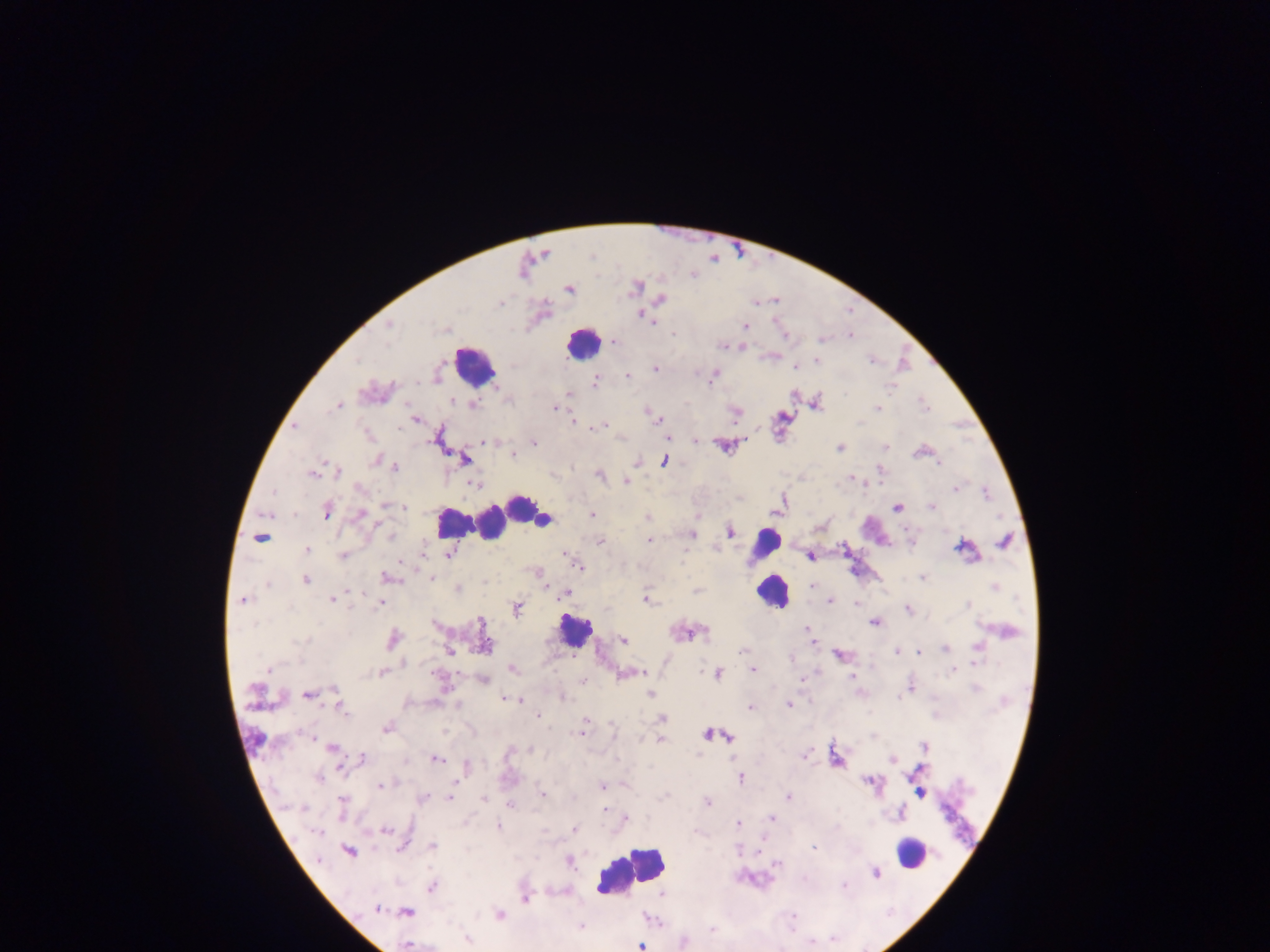
Approximate centers as [x, y] in pixels.
Summary:
  - Plasmodium parasite locations: [592, 256], [634, 287], [569, 289], [661, 299], [500, 303], [643, 316], [650, 321], [389, 325], [745, 326], [785, 335], [850, 335], [821, 339], [613, 341], [721, 346], [816, 360], [357, 361], [871, 361], [656, 368], [794, 368], [713, 375], [627, 376], [595, 382], [891, 387], [567, 395], [452, 402], [474, 404], [817, 404], [924, 405], [337, 406], [555, 409], [877, 409], [649, 412], [734, 413], [655, 417], [415, 420], [573, 420], [602, 426], [295, 427], [667, 437], [696, 441], [485, 442], [533, 443], [724, 445], [886, 446], [840, 447], [513, 455], [464, 460], [376, 461], [665, 461], [939, 464], [395, 467], [880, 470], [337, 472], [312, 473], [600, 475], [852, 478], [626, 481], [474, 484], [360, 489], [955, 489], [272, 492], [986, 493], [388, 506], [931, 507], [404, 508], [898, 508], [327, 512], [592, 514], [361, 515], [267, 516], [647, 518], [820, 526], [731, 532], [691, 534], [390, 535], [259, 538], [600, 541], [649, 541], [1004, 542], [962, 548], [307, 550], [424, 553], [342, 555], [449, 555], [566, 556], [809, 556], [578, 566], [386, 576], [431, 577], [923, 577], [306, 580], [267, 586], [813, 586], [995, 587], [457, 589], [567, 593], [332, 600], [647, 600], [243, 601], [830, 602], [380, 603], [857, 604], [969, 604], [517, 608], [908, 609], [874, 623], [435, 625], [484, 627], [808, 630], [392, 639], [485, 640], [622, 640], [299, 642], [811, 642], [978, 647], [945, 648], [742, 651], [449, 652], [896, 652], [920, 652], [839, 655], [512, 668], [269, 669], [752, 669], [953, 670], [381, 672], [633, 673], [718, 673], [852, 677], [484, 680], [583, 681], [908, 686], [975, 688], [335, 690], [651, 694], [308, 695], [563, 697], [507, 699], [788, 705], [750, 707], [342, 710], [538, 716], [663, 718], [585, 724], [386, 729], [582, 730], [614, 730], [708, 734], [309, 736], [728, 737], [660, 740], [924, 746], [332, 747], [529, 750], [805, 755], [363, 757], [437, 759], [892, 759], [467, 766], [919, 768], [319, 777], [741, 778], [870, 781], [381, 785], [603, 786], [542, 794], [919, 794], [665, 795], [451, 796], [788, 796], [423, 798], [483, 799], [342, 802], [707, 802], [511, 805], [303, 808], [605, 811], [901, 813], [626, 818], [771, 818], [738, 824], [498, 826], [575, 829], [385, 831], [318, 832], [401, 847], [433, 847], [814, 847], [349, 851], [570, 862], [778, 864], [876, 873], [844, 886], [432, 887], [662, 895], [525, 899], [376, 908], [407, 912], [499, 914], [792, 916], [581, 927], [711, 929], [468, 939], [834, 940], [408, 945], [641, 946]
  - Leukocyte locations: [582, 343], [474, 365], [523, 507], [540, 516], [451, 522], [491, 523], [765, 545], [771, 591], [574, 631], [909, 853], [631, 871]
  - Capture: mobile-phone photograph through a microscope
  - Country: Ghana
  - Field of view: single
  - Image size: 1270×952 pixels
  - Preparation: thick blood smear